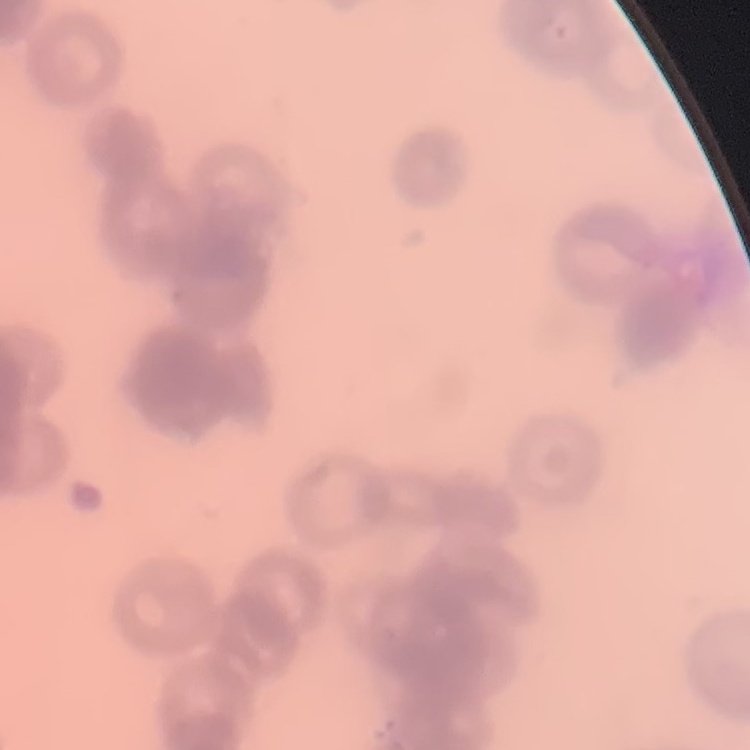

{
  "red_blood_cell_morphology": "rouleaux formation",
  "image_type": "square crop of a larger photomicrograph",
  "preparation": "thin peripheral smear",
  "stain": "Field's or Giemsa"
}